Assess the morphology of the erythrocytes.
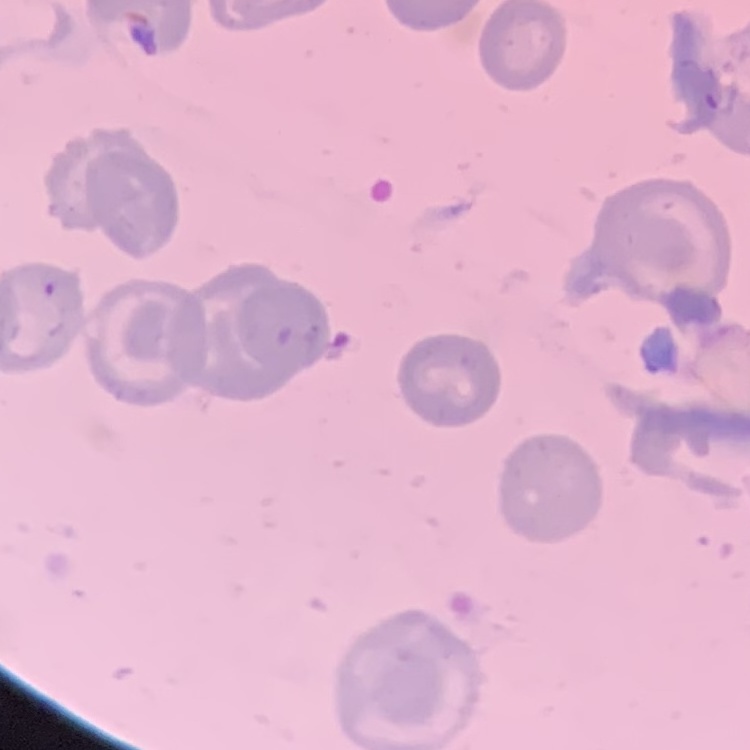

They show no rouleaux formation.

Summary:
  - Image type: one tile cut from a larger photomicrograph
  - Stain: Field's or Giemsa
  - Preparation: thin blood smear